Outline platelets.
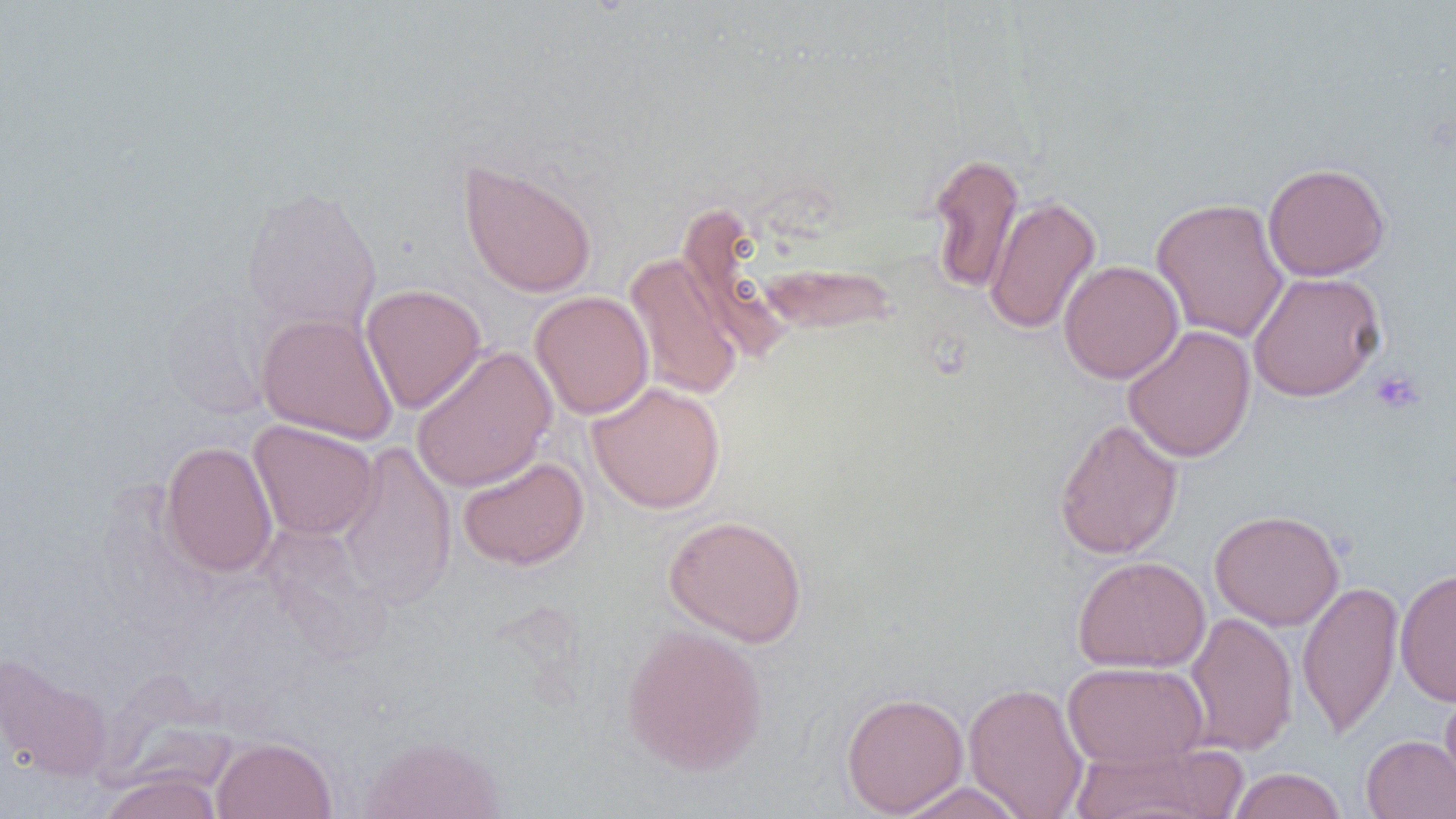
Approximate bounding boxes as [x1, y1, x2, y2] in pixels.
Platelets: [1370, 368, 1425, 415].

Uninfected red blood cell locations: [927, 152, 1024, 294], [458, 158, 598, 299], [1262, 162, 1391, 281], [240, 184, 383, 334], [984, 195, 1101, 336], [1150, 197, 1290, 343], [677, 206, 798, 363], [624, 253, 744, 401], [1058, 260, 1184, 384], [757, 261, 899, 335], [1247, 271, 1386, 402], [360, 283, 487, 414], [162, 289, 276, 421], [530, 291, 654, 419], [255, 312, 398, 444], [1122, 325, 1256, 463], [411, 344, 557, 492], [587, 381, 726, 514], [1054, 417, 1183, 560], [248, 420, 379, 541], [160, 441, 278, 578], [337, 441, 457, 609], [457, 457, 589, 570], [1209, 509, 1345, 631], [663, 514, 808, 647], [1072, 555, 1211, 673], [1395, 567, 1456, 706], [1297, 579, 1404, 739], [1183, 611, 1298, 757], [621, 623, 768, 776], [0, 652, 116, 782], [1062, 661, 1209, 769], [963, 681, 1090, 818], [1440, 684, 1456, 803], [841, 691, 969, 817], [358, 733, 507, 819], [1361, 734, 1456, 819], [211, 736, 337, 818], [1067, 741, 1244, 819], [1228, 767, 1347, 819], [98, 772, 224, 819], [892, 781, 1029, 818]. Slide-level diagnosis: negative for blood parasites. Single field of view. Image is 1456×819 pixels. Thin blood film. 1000x magnification. Light microscopy.